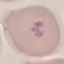

Result: malaria parasites detected. Giemsa-stained preparation. Thin blood film. Automatically extracted cell patch, resized to 64 × 64 pixels. Acquired by smartphone through the microscope eyepiece.